Assess this cell for malaria.
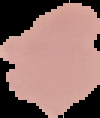
It is uninfected.

Image is 100×118 pixels. From a thin blood smear. Segmented cell region on a black background.